Locate every Plasmodium parasite.
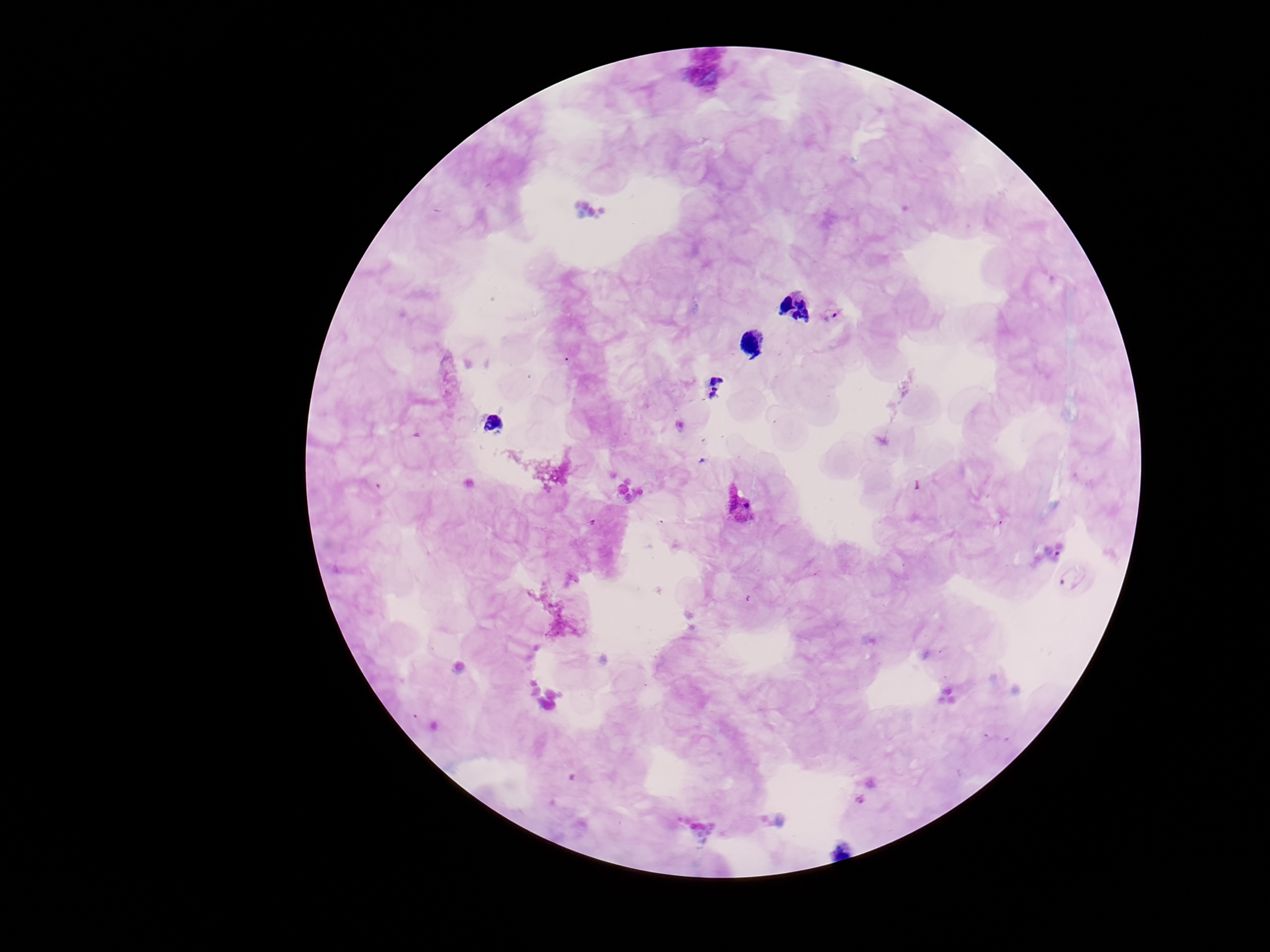
Approximate centers as (x, y) in pixels.
Plasmodium parasites: (834, 312), (738, 508), (1076, 577).

Summary:
  - Magnification: 100x
  - Stain: Giemsa
  - Preparation: thick peripheral-blood smear
  - Capture: smartphone camera through the microscope eyepiece
  - Field of view: one from this slide
  - Patient malaria status: infected
  - Image size: 1270×952 pixels